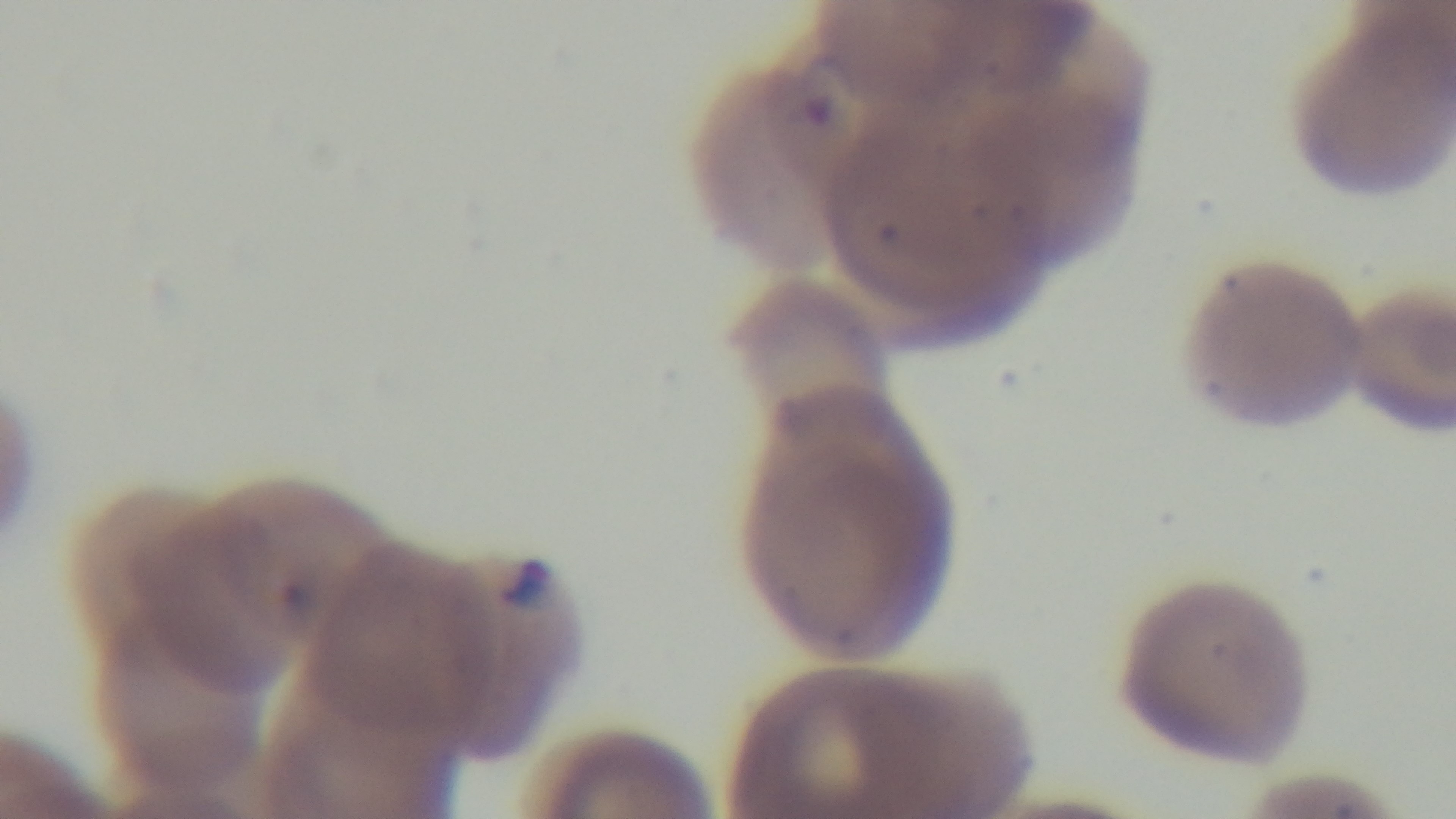

Summary:
  - Field of view: single
  - Capture: mounted 4K digital camera
  - Objective: 100x oil immersion
  - Modality: light microscopy
  - Preparation: thin
  - Malaria status: infected
  - Stain: Giemsa